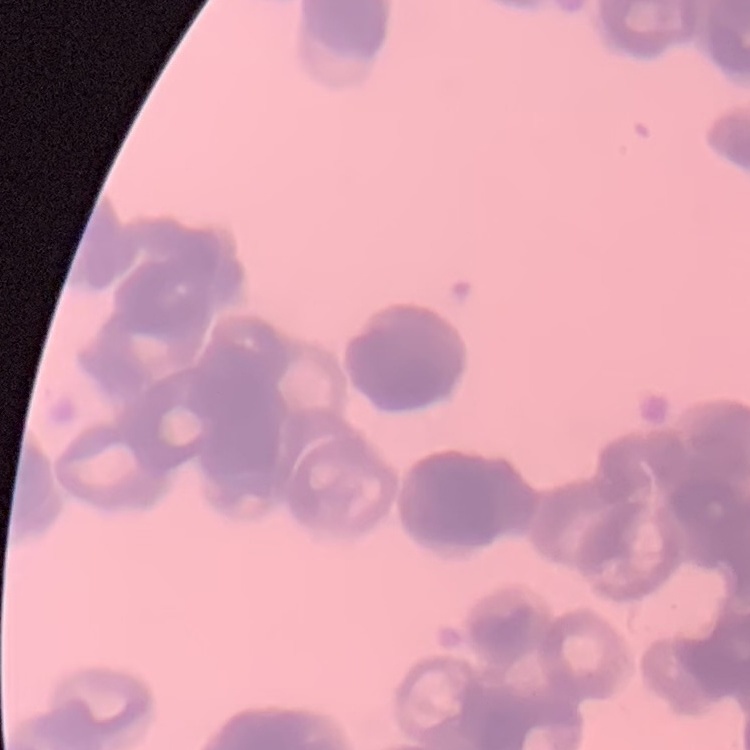

{
  "erythrocyte_morphology": "rouleaux formation",
  "stain": "Field's or Giemsa",
  "image_type": "one tile cut from a larger photomicrograph",
  "preparation": "thin blood smear"
}